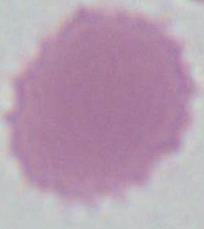 Captured at 1000x magnification. Micrograph. An erythrocyte is shown.